Name the cell type shown.
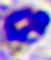
A leukocyte.

magnification = 400x
modality = photomicrograph